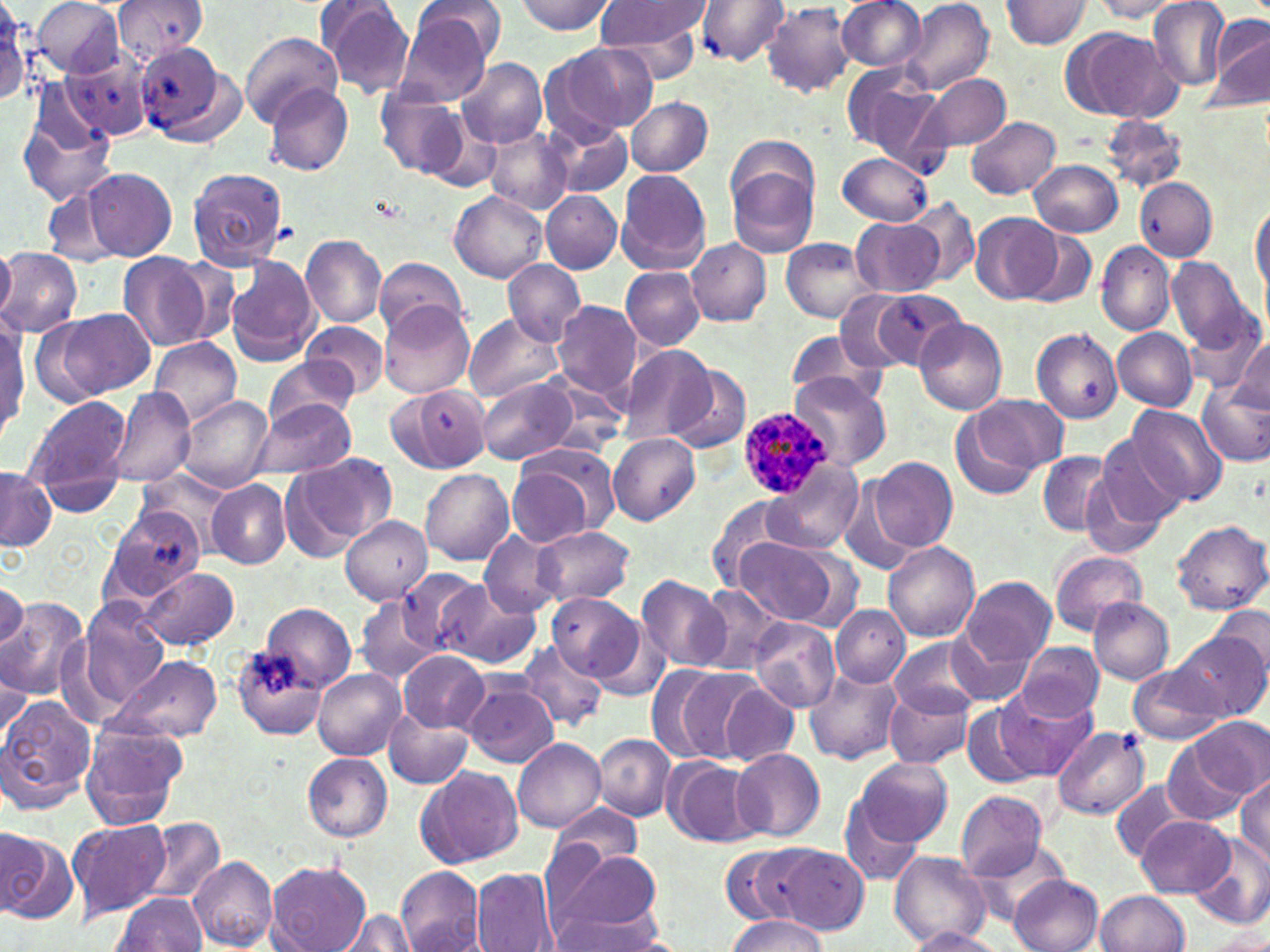
slide-level diagnosis = Plasmodium ovale
modality = optical microscopy
field of view = one of a larger specimen
magnification = 1000x
Plasmodium ovale-infected red blood cell locations = approximate bounding boxes as (x1,y1)-(x2,y2) corner pairs in pixels: (736,406)-(833,499)
stain = May-Grünwald-Giemsa
preparation = thin blood smear
image size = 1270×952 pixels
uninfected red blood cell locations = approximate bounding boxes as (x1,y1)-(x2,y2) corner pairs in pixels: (1,0)-(31,107), (114,0)-(207,62), (513,0)-(615,35), (595,0)-(712,59), (696,0)-(789,66), (837,0)-(927,72), (900,0)-(993,97), (1002,0)-(1092,48), (1091,0)-(1189,20), (1148,0)-(1229,90), (29,1)-(128,80), (316,1)-(415,99), (763,3)-(854,97), (396,4)-(498,105), (1204,13)-(1270,113), (1062,27)-(1180,123), (240,32)-(342,125), (553,41)-(659,136), (132,44)-(241,145), (62,51)-(154,141), (457,57)-(548,148), (843,65)-(950,170), (919,73)-(1010,153), (265,84)-(355,176), (380,89)-(467,176), (15,93)-(119,209), (626,95)-(713,178), (965,115)-(1061,198), (1103,115)-(1188,192), (542,117)-(632,198), (486,128)-(573,214), (836,152)-(933,225), (728,159)-(819,257), (1030,159)-(1123,237), (186,167)-(288,269), (81,168)-(177,261), (615,169)-(710,273), (1136,177)-(1218,260), (450,188)-(548,283), (541,190)-(623,273), (1249,199)-(1269,299), (907,200)-(979,285), (969,213)-(1061,304), (851,219)-(945,298), (1017,225)-(1098,309), (301,236)-(386,327), (781,238)-(873,323), (688,239)-(770,326), (1095,242)-(1175,337), (0,246)-(15,320), (0,248)-(83,338), (118,253)-(210,354), (225,255)-(319,366), (1165,255)-(1256,353), (374,256)-(470,340), (502,259)-(585,346), (621,267)-(704,350), (833,288)-(929,375), (867,290)-(965,370), (552,300)-(640,402), (380,303)-(474,398), (44,307)-(156,402), (461,313)-(563,403), (1196,317)-(1270,406), (0,318)-(27,441), (913,318)-(1006,415), (301,321)-(389,398), (1031,328)-(1123,424), (1112,328)-(1197,410), (786,329)-(884,402), (148,336)-(242,429), (1231,338)-(1269,414), (616,345)-(716,444), (264,360)-(358,431), (667,365)-(751,455), (788,370)-(890,471), (476,378)-(578,465), (1197,378)-(1270,466), (394,384)-(492,473), (106,388)-(196,488), (965,393)-(1066,483), (176,395)-(276,493), (24,396)-(130,511), (250,400)-(357,482), (1125,406)-(1229,506), (951,415)-(1041,500), (1095,431)-(1187,533), (607,433)-(701,524), (506,445)-(616,547), (286,452)-(396,554), (1039,452)-(1114,536), (867,455)-(958,553), (1078,462)-(1171,563), (766,463)-(861,556), (0,469)-(56,553), (421,469)-(513,564), (138,471)-(231,552), (206,479)-(291,570), (837,480)-(919,577), (707,494)-(797,590), (100,506)-(205,606), (340,515)-(433,606), (1171,520)-(1270,614), (532,526)-(634,606), (478,531)-(567,619), (735,536)-(843,626), (883,542)-(980,641), (1050,550)-(1146,636), (136,567)-(237,650), (397,568)-(485,655), (635,575)-(732,672), (959,575)-(1055,669), (0,578)-(28,652), (436,580)-(541,670), (693,583)-(789,674), (548,592)-(646,683), (355,593)-(442,685), (1089,597)-(1174,684), (0,599)-(87,699), (77,599)-(166,708), (1211,602)-(1270,684), (262,603)-(356,693), (831,604)-(908,687), (749,618)-(841,713), (1174,626)-(1266,721), (945,632)-(1035,706), (890,637)-(987,718), (508,638)-(599,815), (516,641)-(607,731), (1016,642)-(1105,722), (233,646)-(328,739), (398,650)-(488,732), (106,655)-(223,743), (0,660)-(31,752), (1127,664)-(1226,745), (659,665)-(762,764), (803,668)-(901,766), (313,669)-(406,760), (462,677)-(559,767), (720,683)-(799,766), (885,687)-(976,770), (991,688)-(1096,782), (0,691)-(96,814), (960,700)-(1048,789), (383,709)-(473,788), (1186,717)-(1269,804), (81,721)-(188,832), (1051,725)-(1149,819), (595,734)-(674,820), (513,739)-(605,832), (1162,739)-(1255,827), (732,749)-(825,841), (303,754)-(393,842), (853,756)-(953,847), (663,757)-(760,850), (1214,759)-(1270,845), (416,766)-(522,866), (1235,775)-(1269,862), (1110,779)-(1201,860), (954,790)-(1047,882), (837,798)-(926,884), (549,802)-(644,872), (1136,816)-(1233,896), (139,818)-(225,908), (67,819)-(170,919), (0,827)-(73,924), (1190,830)-(1270,929), (966,836)-(1072,926), (752,843)-(869,932), (721,846)-(802,925), (550,851)-(665,937), (889,851)-(989,949), (188,854)-(277,950), (266,860)-(370,952), (396,868)-(486,952), (471,869)-(558,952), (1009,874)-(1104,952), (1095,891)-(1191,952), (112,893)-(206,951), (547,907)-(670,952), (337,909)-(417,952), (725,915)-(827,951), (904,928)-(1008,952), (1199,930)-(1270,951)